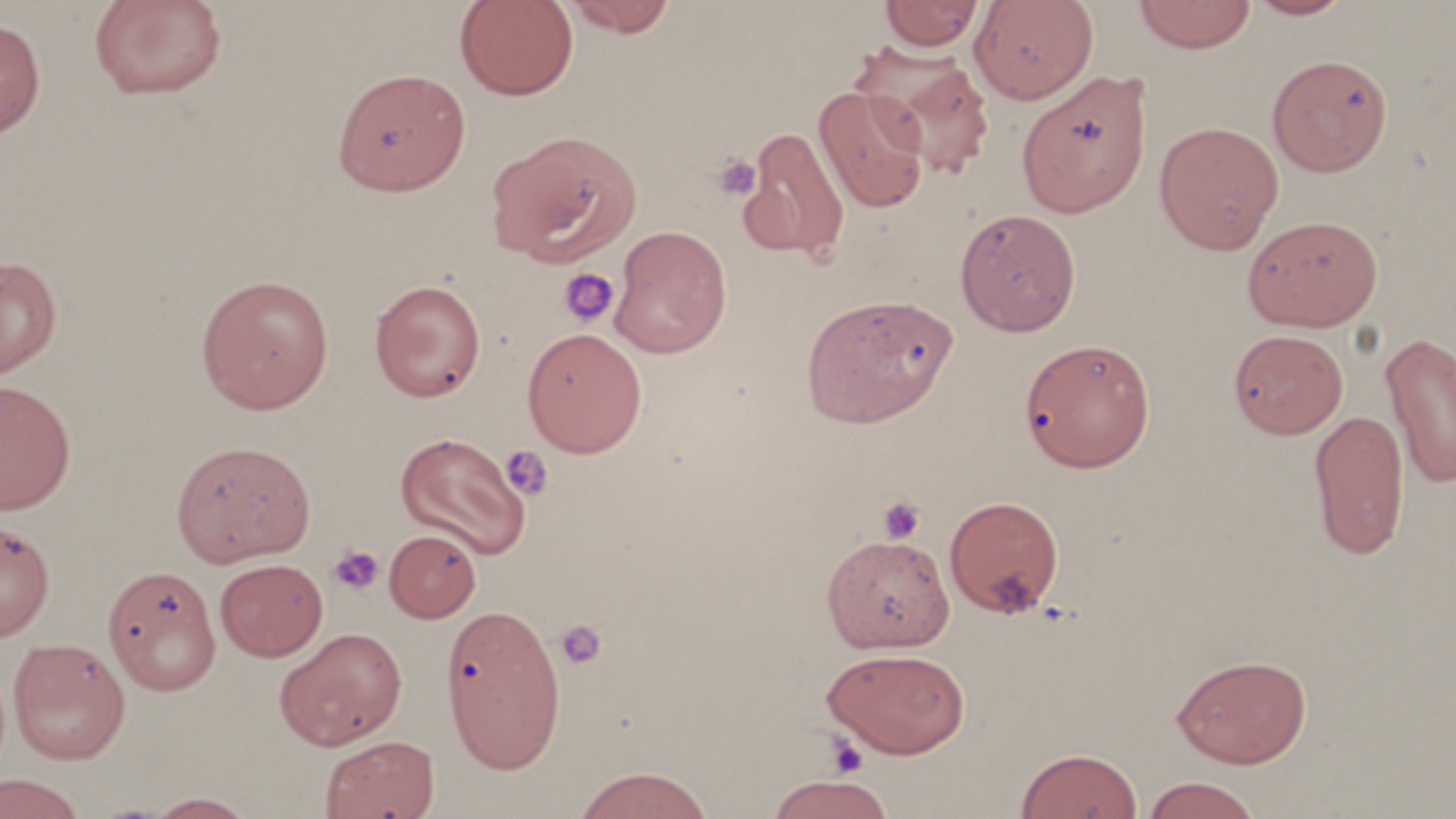

Summary:
  - Coordinate format: approximate bounding boxes as named x1/y1/x2/y2 corners in pixels
  - Uninfected red blood cell locations: (x1=89, y1=0, x2=227, y2=101), (x1=454, y1=0, x2=579, y2=100), (x1=560, y1=0, x2=678, y2=37), (x1=969, y1=0, x2=1098, y2=104), (x1=1132, y1=0, x2=1257, y2=53), (x1=1243, y1=0, x2=1356, y2=20), (x1=880, y1=1, x2=985, y2=51), (x1=0, y1=17, x2=46, y2=140), (x1=850, y1=44, x2=995, y2=178), (x1=1267, y1=53, x2=1393, y2=177), (x1=334, y1=68, x2=470, y2=196), (x1=1016, y1=70, x2=1153, y2=218), (x1=813, y1=86, x2=931, y2=214), (x1=1154, y1=121, x2=1285, y2=254), (x1=738, y1=126, x2=851, y2=262), (x1=485, y1=130, x2=641, y2=268), (x1=955, y1=208, x2=1081, y2=335), (x1=1242, y1=214, x2=1383, y2=331), (x1=608, y1=225, x2=732, y2=359), (x1=0, y1=255, x2=61, y2=379), (x1=195, y1=273, x2=334, y2=414), (x1=369, y1=279, x2=487, y2=402), (x1=800, y1=294, x2=957, y2=428), (x1=521, y1=327, x2=648, y2=457), (x1=1228, y1=329, x2=1348, y2=439), (x1=1380, y1=331, x2=1456, y2=491), (x1=1020, y1=337, x2=1155, y2=472), (x1=0, y1=379, x2=77, y2=515), (x1=1308, y1=408, x2=1410, y2=561), (x1=394, y1=432, x2=531, y2=559), (x1=170, y1=440, x2=315, y2=567), (x1=944, y1=495, x2=1065, y2=618), (x1=0, y1=519, x2=55, y2=641), (x1=385, y1=529, x2=481, y2=622), (x1=821, y1=533, x2=955, y2=653), (x1=215, y1=558, x2=327, y2=661), (x1=102, y1=564, x2=221, y2=696), (x1=434, y1=600, x2=559, y2=771), (x1=274, y1=627, x2=407, y2=750), (x1=8, y1=637, x2=131, y2=764), (x1=822, y1=646, x2=971, y2=758), (x1=1172, y1=654, x2=1312, y2=768), (x1=318, y1=734, x2=439, y2=819), (x1=1016, y1=747, x2=1143, y2=819), (x1=572, y1=765, x2=715, y2=819), (x1=0, y1=772, x2=87, y2=818), (x1=766, y1=774, x2=896, y2=818), (x1=1140, y1=776, x2=1263, y2=819), (x1=142, y1=791, x2=257, y2=818)
  - Platelet locations: (x1=711, y1=153, x2=762, y2=201), (x1=558, y1=266, x2=620, y2=329), (x1=500, y1=445, x2=554, y2=500), (x1=878, y1=495, x2=925, y2=543), (x1=327, y1=545, x2=384, y2=595), (x1=555, y1=620, x2=607, y2=669), (x1=824, y1=734, x2=869, y2=778)
  - Slide-level diagnosis: negative for blood parasites
  - Preparation: thin blood film
  - Image size: 1456×819 pixels
  - Modality: optical microscopy
  - Field of view: one of a larger specimen
  - Stain: May-Grünwald-Giemsa
  - Magnification: 1000x